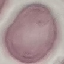

Summary:
  - Malaria status: uninfected
  - Preparation: thin blood film
  - Stain: Giemsa
  - Capture: smartphone camera at the microscope eyepiece
  - Image type: cell patch, automatically extracted from a larger field of view and resized to 64 × 64 pixels